Report the malaria status of this cell.
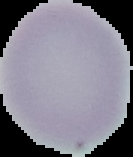
Uninfected.

Image is 133×157 pixels. From a thin blood film. Cell region segmented out of the field of view; the surrounding area is masked to black.